Report the malaria status of this cell.
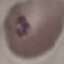
It is parasitized.

Summary:
  - Image type: automatically extracted cell patch, resized to 64 × 64 pixels
  - Preparation: thin blood film
  - Capture: smartphone camera at the microscope eyepiece
  - Stain: Giemsa